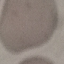
Result: no malaria parasites detected. Giemsa stain. Acquired by smartphone through the microscope eyepiece. Cell patch, automatically extracted from a larger field of view and resized to 64 × 64 pixels. Thin blood film.